Name the parasite shown.
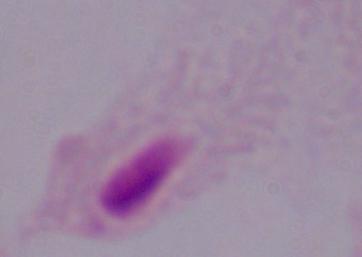

A trichomonad.

Summary:
  - Magnification: 1000x
  - Modality: photomicrograph